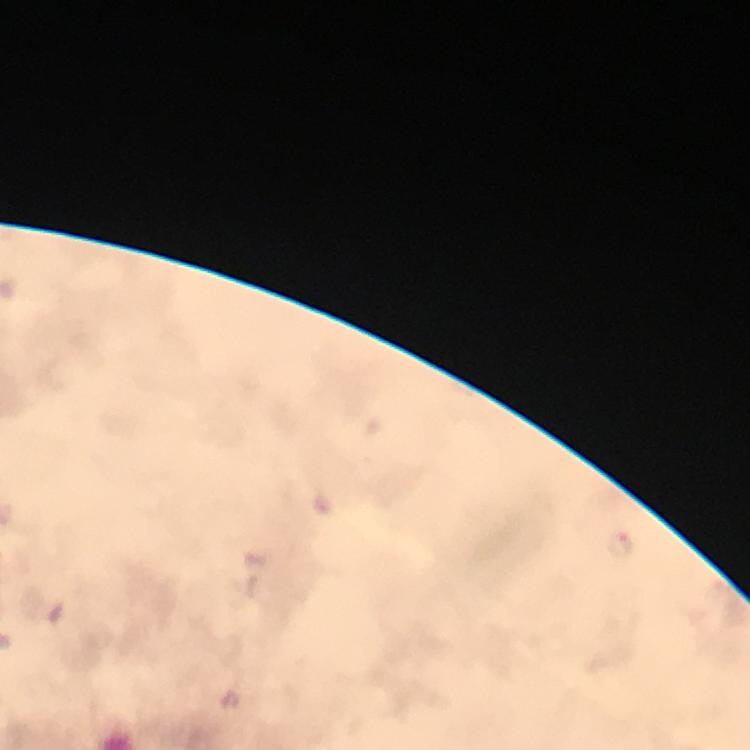 Approximate centers as [x, y] in pixels. Malaria parasite locations: [620, 545]. 100x magnification. Thick smear. Cropped region of a single field of view. Giemsa stain. Image is 750×750 pixels. From a diagnostic examination for malaria. Immersion oil was used. Smartphone photograph taken through a microscope.